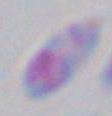
{
  "identification": "Toxoplasma gondii",
  "modality": "photomicrograph",
  "magnification": "1000x"
}